Assess this cell for malaria.
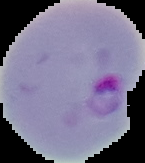

It is parasitized.

Segmented cell region on a black background. Image is 145×163 pixels. From a thin blood smear.